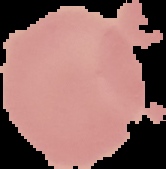 Result: no malaria parasites detected. From a thin blood smear. Cell region segmented out of the field of view; the surrounding area is masked to black. Image is 166×169 pixels.